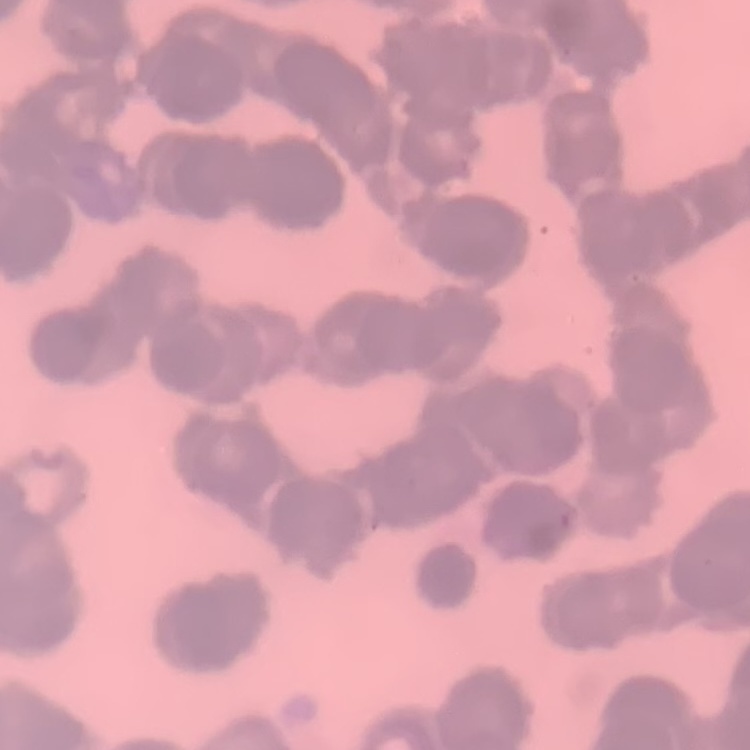 The erythrocytes show rouleaux formation. Thin blood film. Square crop of a larger photomicrograph. Field's or Giemsa stain.